Report the malaria status of this cell.
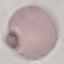
Uninfected.

Giemsa-stained preparation. Photographed with a smartphone camera at the microscope eyepiece. Automatically extracted cell patch, resized to 64 × 64 pixels. Thin blood film.